State which parasite is depicted.
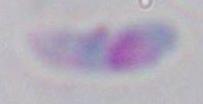

Toxoplasma gondii.

Captured at 1000x magnification. Micrograph.